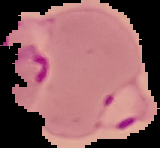

image type = cell region segmented out of the field of view; surrounding area masked to black
malaria status = parasitized
preparation = thin blood film
image size = 160×148 pixels